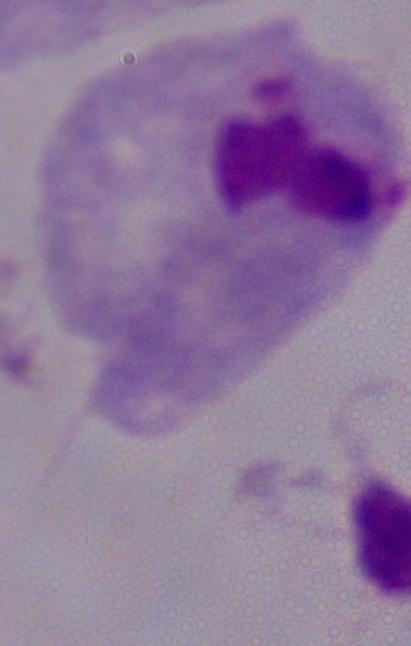

magnification = 1000x
identification = trichomonad
modality = micrograph